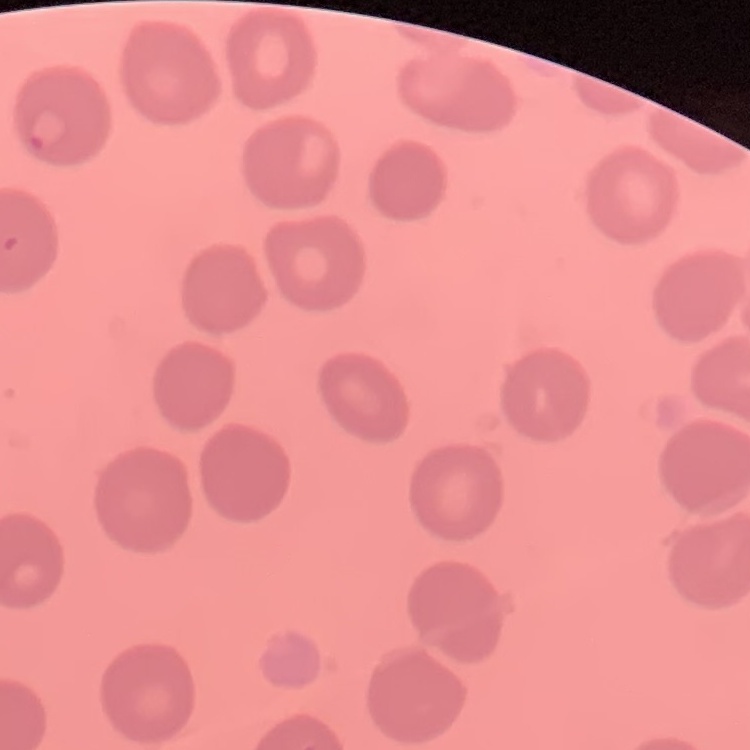

erythrocyte_morphology: no rouleaux formation
preparation: thin peripheral smear
stain: Field's or Giemsa
image_type: square crop of a larger photomicrograph